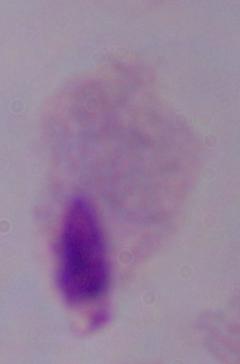 A trichomonad is shown. 1000x magnification. Micrograph.